Name the parasite shown.
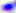
This is Toxoplasma gondii.

Summary:
  - Modality: micrograph
  - Magnification: 400x